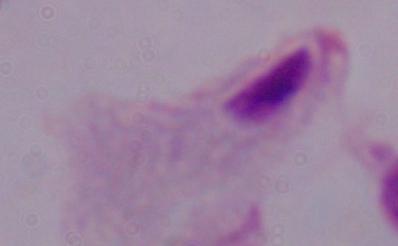
{
  "identification": "trichomonad",
  "magnification": "1000x",
  "modality": "photomicrograph"
}